Name the cell type shown.
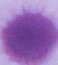
This is an erythrocyte.

Micrograph. Captured at 1000x magnification.